Assess this cell for malaria.
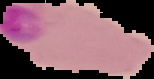
It is parasitized.

image size = 154×79 pixels
preparation = thin blood film
image type = segmented cell region on a black background